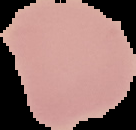
{
  "preparation": "thin blood film",
  "image_type": "segmented cell region with the area outside set to black",
  "malaria_status": "uninfected",
  "image_size": "136×130 pixels"
}